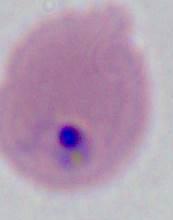

400x or 1000x magnification. A Plasmodium parasite is seen. Micrograph.